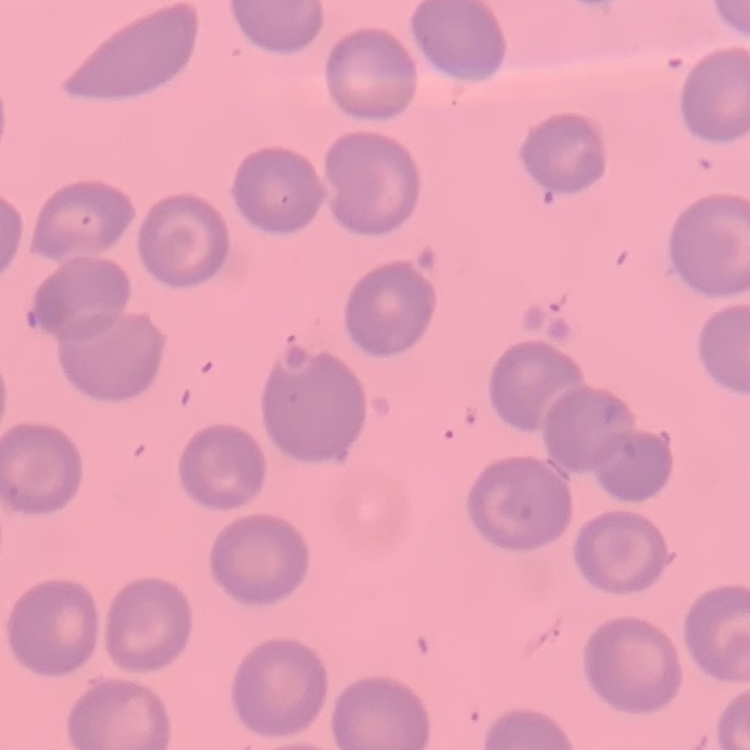

erythrocyte morphology = no rouleaux formation
preparation = thin blood smear
stain = Field's or Giemsa
image type = square crop of a larger photomicrograph